Report the malaria status.
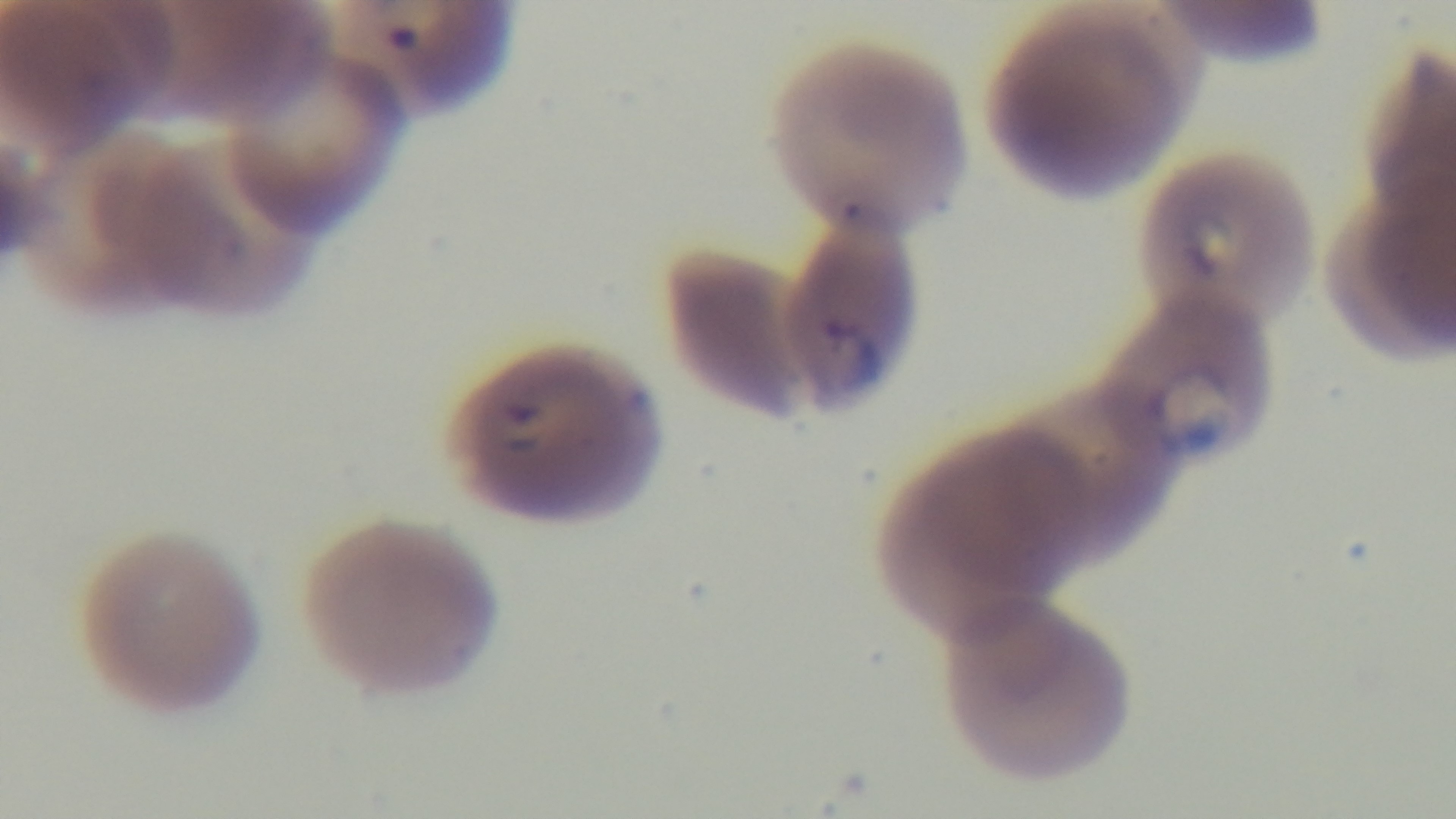

It is infected.

modality = light microscopy
field of view = one from the slide
capture = mounted 4K digital camera
stain = Giemsa
preparation = thin blood film
objective = 100x oil immersion